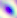
Summary:
  - Modality: micrograph
  - Magnification: 400x
  - Identification: Toxoplasma gondii